Report the malaria status of this cell.
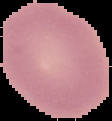

Uninfected.

Summary:
  - Preparation: thin blood smear
  - Image type: segmented cell region on a black background
  - Image size: 112×121 pixels